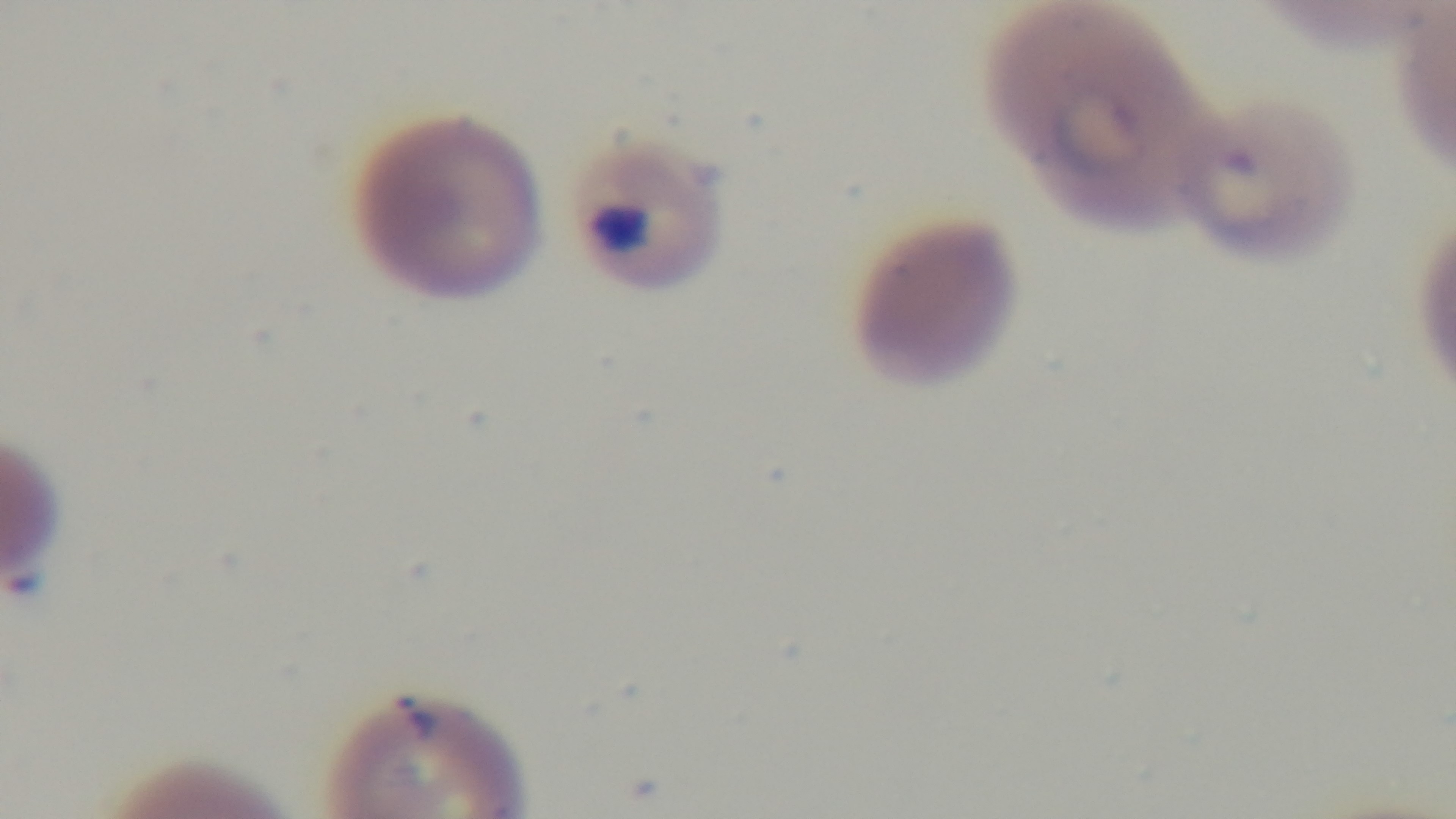 Photomicrograph. Single field of view. Giemsa-stained. Oil-immersion objective, 100x. Mounted 4K digital camera. Preparation: thin blood film. Malaria status: positive.